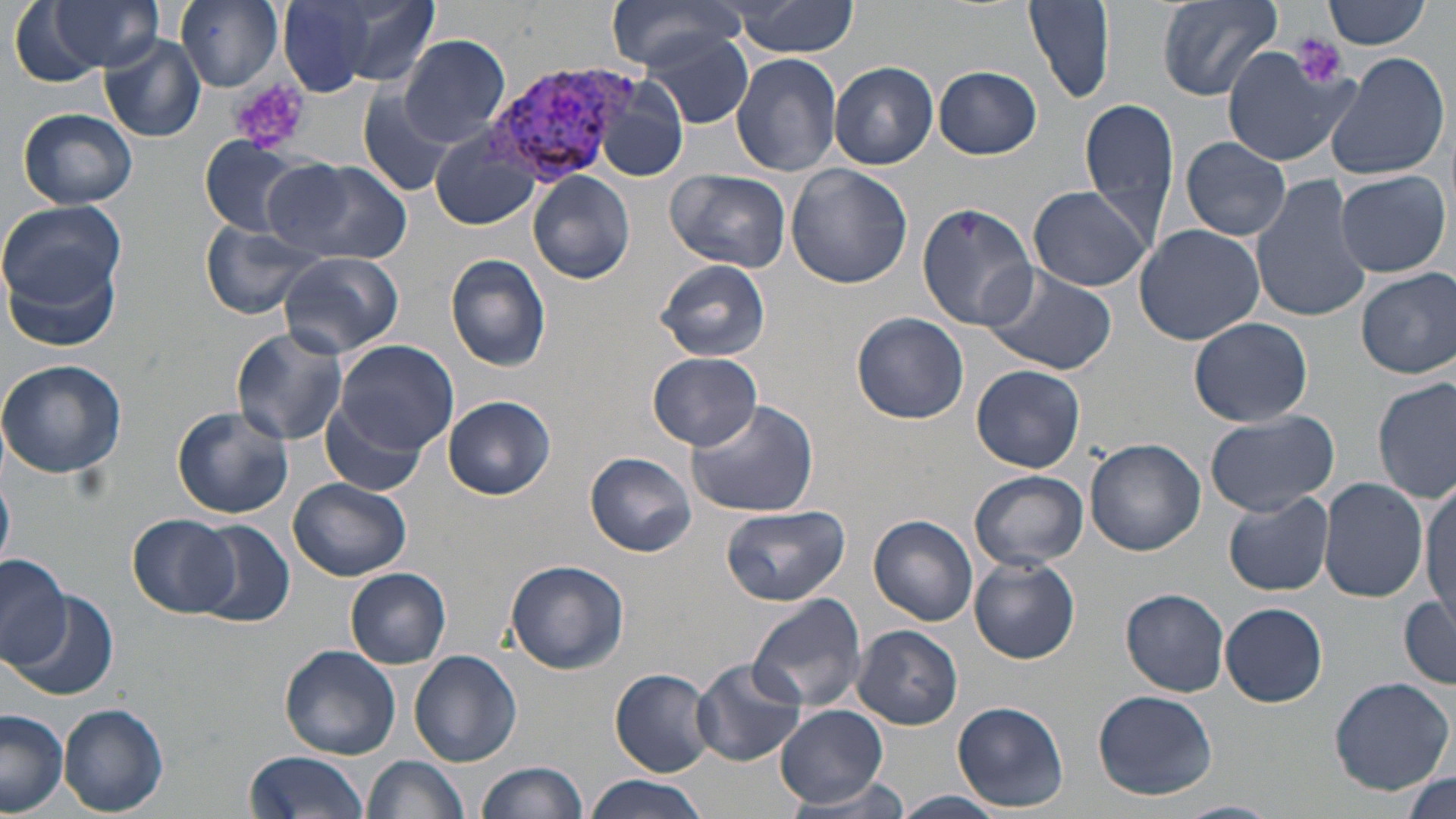

slide_level_diagnosis: Plasmodium vivax
stain: May-Grünwald-Giemsa
platelet_locations: 'approximate bounding boxes as (x1, y1, x2, y2) in pixels: (1290, 34, 1348, 89), (230, 77, 311, 152)'
plasmodium_vivax_infected_red_blood_cell_locations: 'approximate bounding boxes as (x1, y1, x2, y2) in pixels: (485, 64, 630, 186)'
modality: light microscopy
preparation: thin blood smear
image_size: 1456×819 pixels
uninfected_red_blood_cell_locations: 'approximate bounding boxes as (x1, y1, x2, y2) in pixels: (41, 0, 163, 73), (177, 0, 284, 90), (605, 0, 750, 70), (1024, 0, 1115, 105), (1157, 0, 1285, 100), (1325, 0, 1429, 48), (273, 1, 421, 97), (731, 1, 861, 59), (638, 33, 759, 127), (98, 34, 207, 143), (399, 35, 509, 146), (1221, 47, 1355, 166), (730, 53, 843, 175), (1324, 53, 1449, 182), (828, 62, 938, 169), (934, 65, 1043, 160), (595, 78, 687, 182), (358, 90, 454, 197), (1082, 97, 1180, 242), (16, 108, 140, 209), (433, 129, 542, 231), (199, 137, 304, 236), (1179, 137, 1291, 240), (268, 157, 413, 265), (785, 163, 913, 289), (664, 168, 791, 273), (1334, 169, 1451, 278), (528, 170, 637, 284), (1249, 172, 1374, 325), (1028, 185, 1154, 293), (0, 198, 126, 307), (915, 201, 1036, 329), (199, 220, 325, 318), (1134, 224, 1265, 346), (277, 252, 403, 358), (4, 253, 122, 354), (446, 253, 552, 371), (653, 259, 774, 363), (982, 267, 1117, 375), (1355, 267, 1456, 378), (851, 312, 968, 424), (1188, 316, 1313, 426), (229, 326, 348, 447), (334, 338, 459, 453), (197, 339, 329, 503), (648, 352, 763, 449), (0, 358, 127, 480), (971, 365, 1087, 472), (1373, 375, 1455, 503), (443, 396, 555, 499), (684, 398, 820, 517), (319, 401, 426, 495), (171, 405, 294, 519), (1203, 411, 1340, 517), (1085, 437, 1205, 555), (585, 451, 696, 557), (968, 469, 1089, 571), (289, 477, 414, 582), (1319, 478, 1429, 606), (0, 480, 14, 569), (1421, 481, 1455, 627), (1223, 490, 1335, 597), (720, 505, 851, 606), (128, 514, 240, 617), (869, 514, 979, 627), (189, 521, 293, 627), (0, 553, 71, 669), (505, 558, 630, 675), (968, 558, 1080, 663), (345, 567, 451, 669), (1121, 588, 1232, 695), (8, 590, 119, 703), (747, 594, 869, 715), (1399, 596, 1456, 687), (1221, 602, 1328, 707), (853, 626, 963, 731), (279, 645, 400, 759), (409, 650, 522, 767), (692, 656, 805, 768), (610, 668, 717, 776), (1328, 677, 1454, 794), (1094, 689, 1218, 800), (952, 701, 1069, 811), (59, 703, 169, 817), (776, 704, 887, 808), (0, 709, 69, 816), (243, 751, 371, 819), (365, 755, 470, 819), (477, 760, 588, 818), (1405, 771, 1454, 816), (584, 775, 709, 819), (783, 777, 913, 815), (893, 791, 1006, 818), (1168, 801, 1283, 819)'
field_of_view: one of a larger specimen
magnification: 1000x